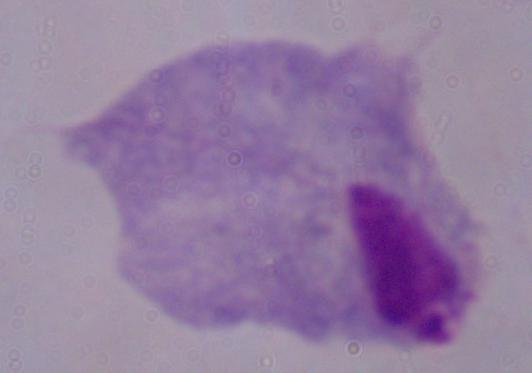
Summary:
  - Magnification: 1000x
  - Modality: micrograph
  - Identification: trichomonad